Classify this cell by malaria status.
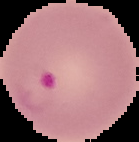

It is parasitized.

Segmented cell region on a black background. Image is 139×142 pixels. From a thin blood smear.